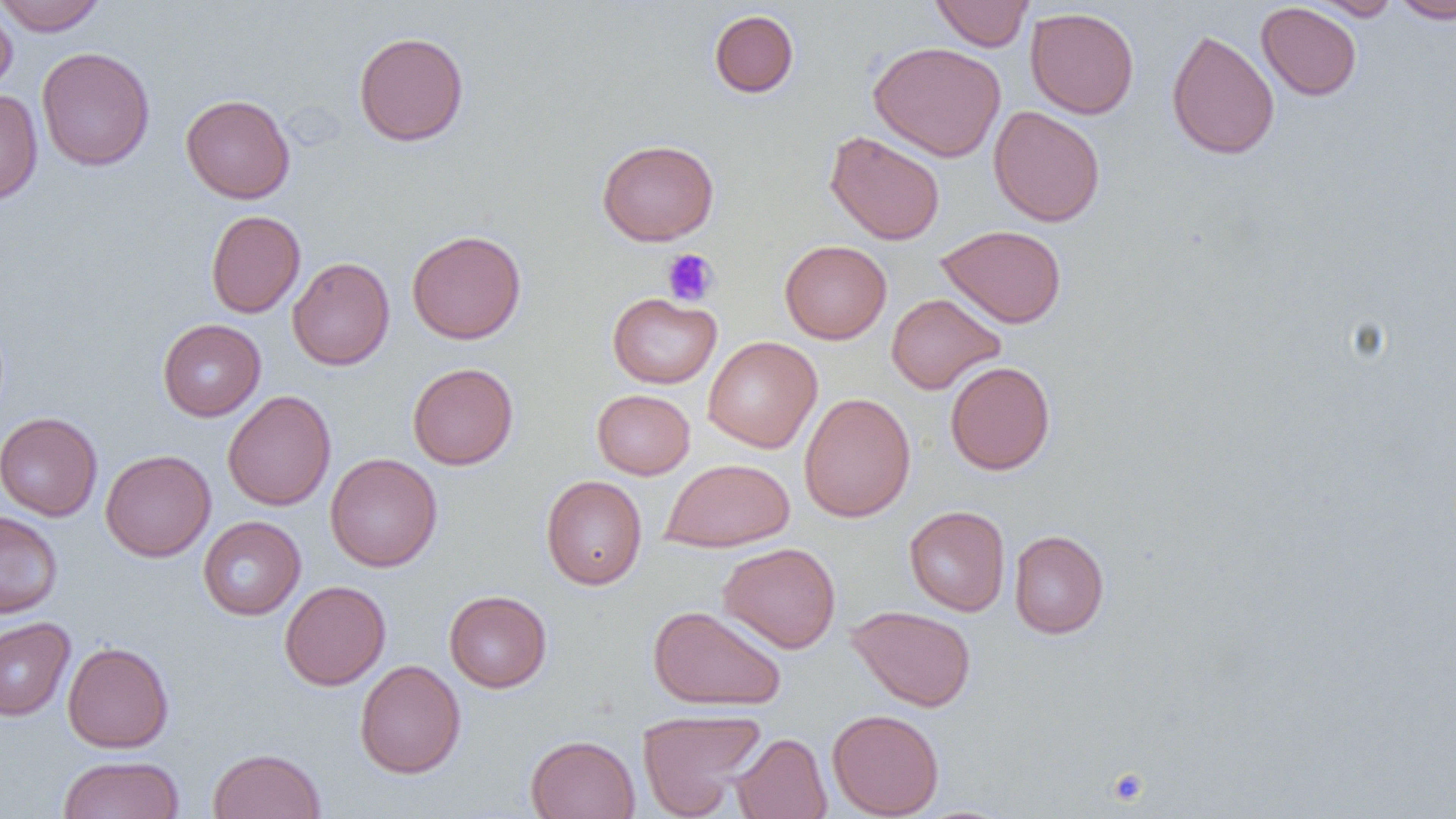
Approximate bounding boxes as (x1,y1)-(x2,y2) corner pairs in pixels. Platelet locations: (662,248)-(719,306), (1106,767)-(1150,806). Uninfected red blood cell locations: (0,0)-(107,35), (930,0)-(1034,51), (1310,0)-(1402,21), (1391,0)-(1456,24), (1256,2)-(1362,101), (0,3)-(17,93), (1025,6)-(1139,119), (709,9)-(799,98), (1166,28)-(1280,160), (353,31)-(469,147), (868,41)-(1006,161), (37,46)-(155,172), (0,88)-(43,206), (181,93)-(295,203), (988,105)-(1105,226), (824,131)-(946,245), (597,139)-(719,245), (206,210)-(305,318), (935,224)-(1067,328), (406,229)-(526,344), (779,240)-(892,344), (288,257)-(395,370), (607,292)-(721,388), (886,293)-(1005,394), (157,318)-(266,421), (703,336)-(822,452), (944,360)-(1055,475), (407,363)-(519,469), (592,389)-(695,479), (223,390)-(337,511), (798,392)-(916,522), (0,412)-(103,521), (100,449)-(216,562), (325,452)-(442,572), (659,458)-(795,552), (541,475)-(647,590), (904,505)-(1010,616), (0,510)-(63,619), (198,516)-(305,620), (1009,530)-(1109,639), (718,542)-(841,653), (279,581)-(391,690), (444,589)-(552,692), (648,605)-(786,711), (847,605)-(977,711), (0,617)-(75,721), (62,641)-(174,753), (354,659)-(466,779), (637,709)-(765,818), (827,709)-(944,818), (732,732)-(832,819), (526,734)-(640,819), (208,748)-(326,819), (58,755)-(185,819). Slide-level diagnosis: no evidence of blood parasites. Thin blood smear. Captured at 1000x magnification. Image is 1456×819 pixels. Optical microscopy. One field of a larger specimen.